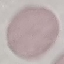

malaria status = uninfected
capture = smartphone camera at the microscope eyepiece
preparation = thin blood film
stain = Giemsa
image type = cell patch, automatically extracted from a larger field of view and resized to 64 × 64 pixels